Describe the morphology of the erythrocytes.
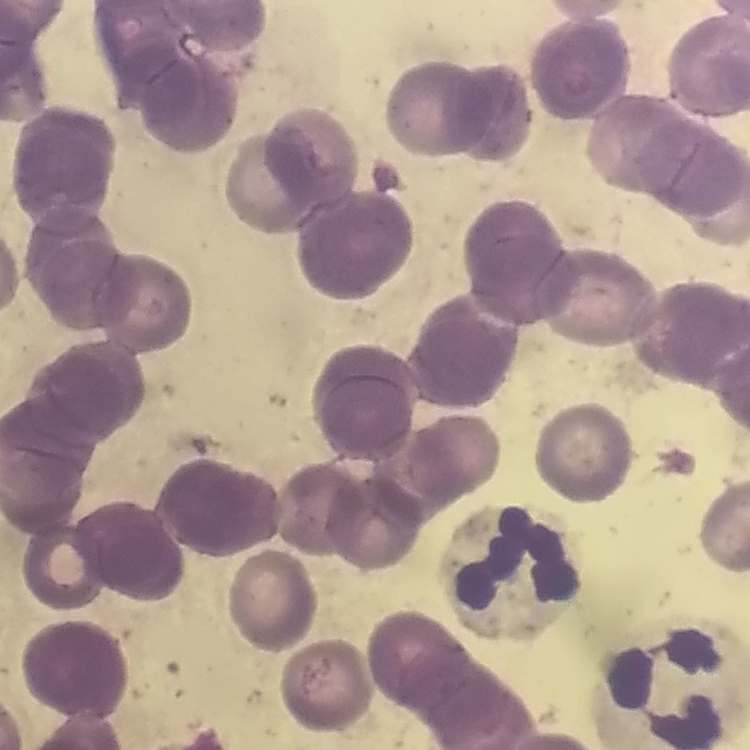

They show rouleaux formation.

One tile cut from a larger photomicrograph. Stained with either Field's or Giemsa. Thin blood smear.